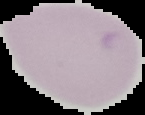

result = no malaria parasites detected
image type = segmented cell region on a black background
preparation = thin blood smear
image size = 145×115 pixels